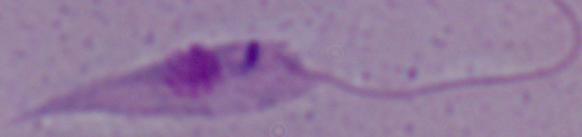

identification = Leishmania
magnification = 1000x
modality = micrograph